Classify this cell by malaria status.
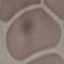
It is uninfected.

stain = Giemsa
image type = cell patch, automatically extracted from a larger field of view and resized to 64 × 64 pixels
preparation = thin blood film
capture = smartphone camera at the microscope eyepiece